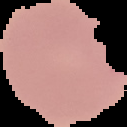

result = malaria parasites identified
image size = 127×127 pixels
image type = segmented cell region with the area outside set to black
preparation = thin blood film